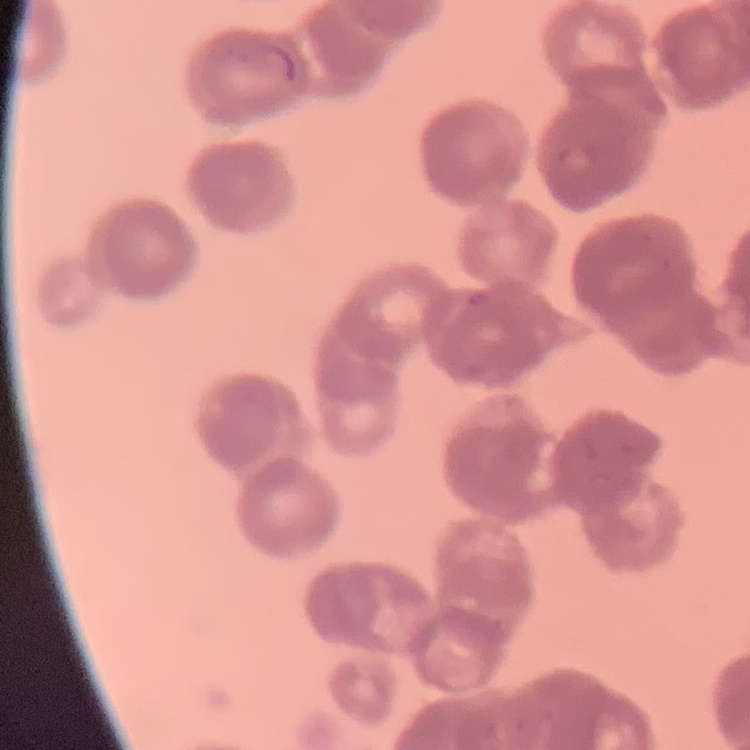

red blood cell morphology = rouleaux formation
stain = Field's or Giemsa
preparation = thin blood smear
image type = one tile cut from a larger photomicrograph